Give the position of every Plasmodium parasite visible.
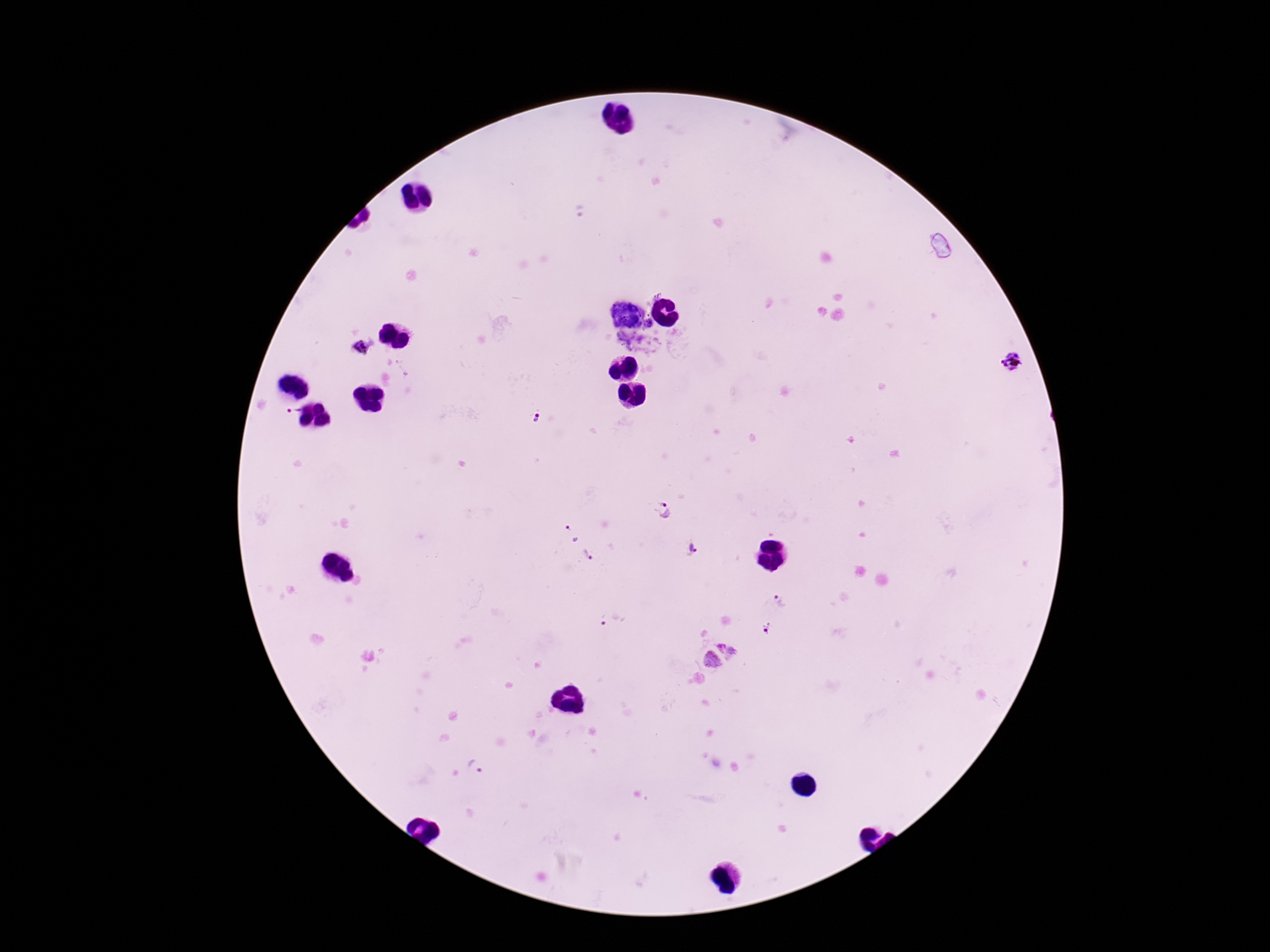

Approximate object centers, in pixels from the top-left corner.
Plasmodium parasites: (x=577, y=210), (x=624, y=313), (x=650, y=324), (x=360, y=348), (x=1012, y=364), (x=294, y=409), (x=537, y=418), (x=663, y=509), (x=570, y=535), (x=692, y=549), (x=588, y=554), (x=781, y=601), (x=609, y=621), (x=766, y=628), (x=721, y=647), (x=733, y=653), (x=711, y=660), (x=475, y=767).

Image is 1270×952 pixels. One field from this slide. Photographed through the microscope eyepiece with a smartphone camera. 100x magnification. Thick blood film. Patient malaria status: infected. Giemsa-stained preparation.